Assess the morphology of the erythrocytes.
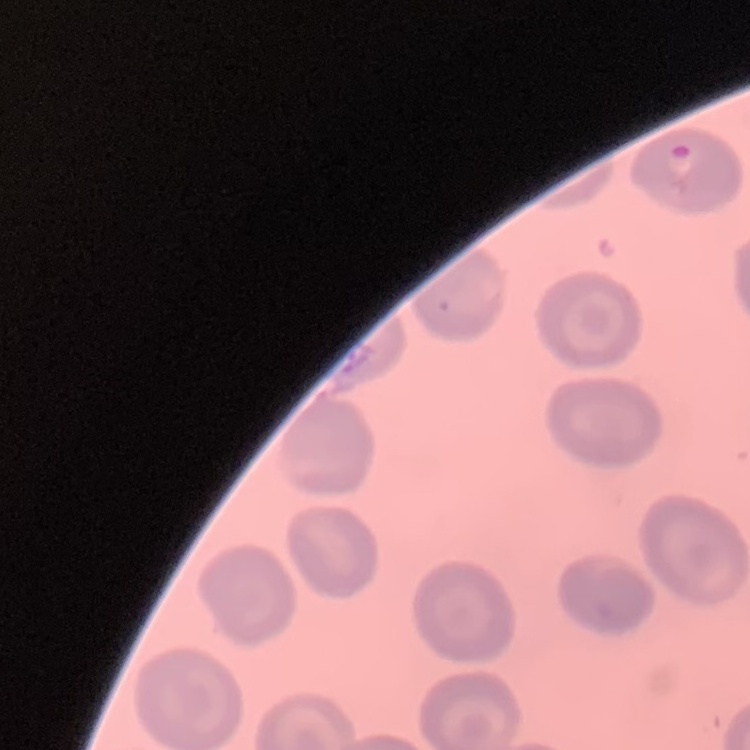
No rouleaux formation.

Thin peripheral smear. Field's or Giemsa stain. Square crop of a larger photomicrograph.